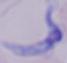

{
  "modality": "photomicrograph",
  "magnification": "1000x",
  "identification": "trypanosome"
}